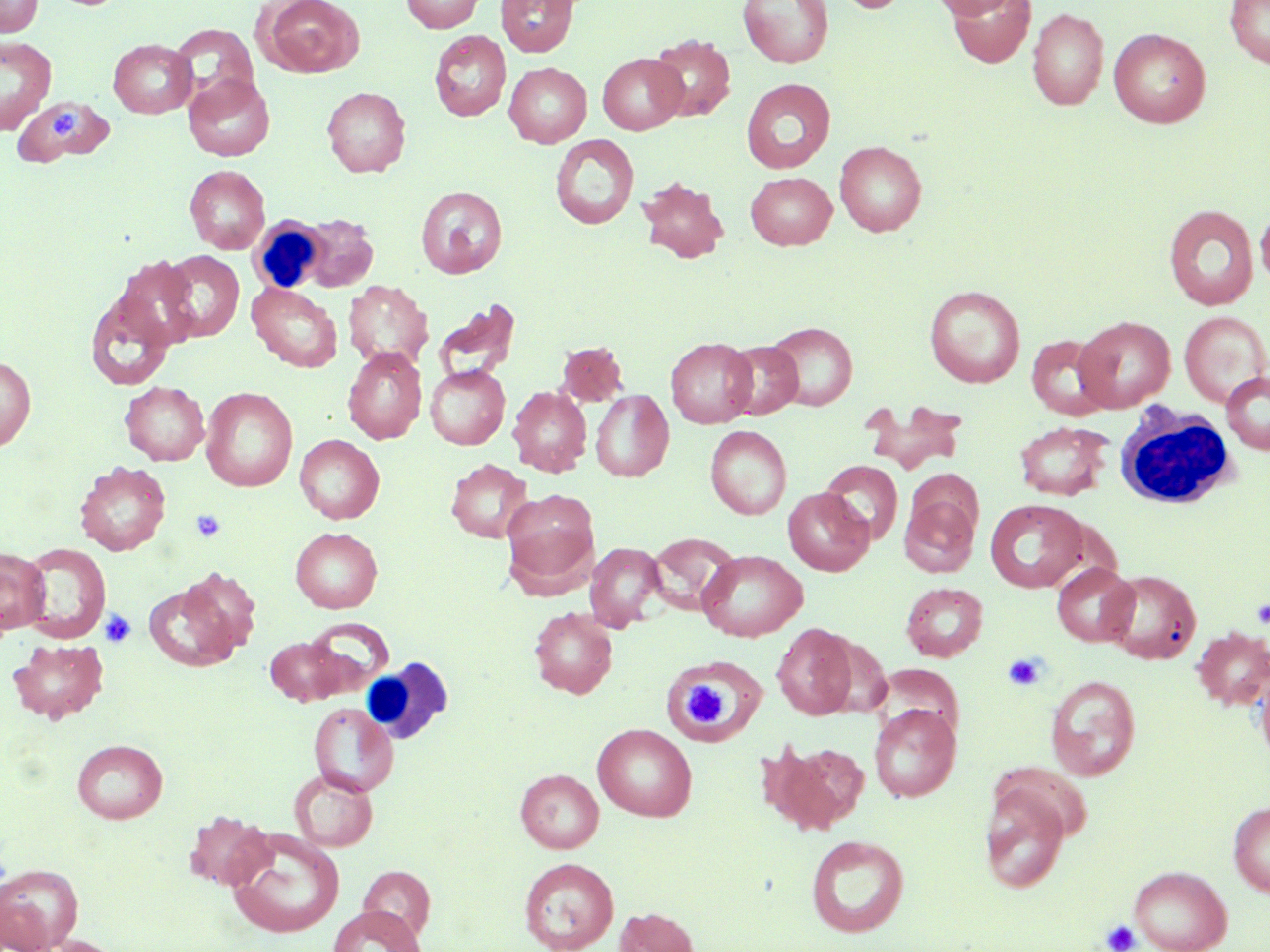
Summary:
  - Coordinate format: approximate bounding boxes as (x1,y1)-(x2,y2) corner pairs in pixels
  - White blood cell locations: (249,216)-(330,295), (1115,401)-(1241,510), (361,657)-(453,746)
  - Platelet locations: (191,509)-(226,542), (1251,599)-(1270,628), (99,610)-(136,647), (1002,652)-(1047,692), (685,681)-(726,726), (1101,919)-(1141,952)
  - Uninfected red blood cell locations: (0,0)-(42,36), (257,0)-(364,78), (401,0)-(485,32), (496,0)-(579,57), (739,0)-(833,68), (829,0)-(910,14), (930,0)-(1018,19), (1225,0)-(1270,68), (946,1)-(1035,68), (1027,6)-(1108,111), (169,22)-(259,105), (1108,28)-(1211,128), (429,29)-(511,121), (648,34)-(736,122), (0,36)-(55,134), (109,38)-(197,118), (598,53)-(687,135), (504,62)-(591,147), (183,74)-(275,161), (741,78)-(835,173), (322,86)-(410,177), (14,96)-(114,167), (550,133)-(639,230), (835,140)-(926,236), (184,165)-(269,254), (745,172)-(837,249), (638,177)-(728,263), (416,186)-(507,278), (1163,203)-(1258,310), (1256,207)-(1270,291), (298,212)-(378,292), (160,250)-(244,342), (115,257)-(198,348), (342,280)-(432,371), (247,282)-(343,372), (924,284)-(1025,387), (85,290)-(176,391), (432,297)-(522,385), (1179,310)-(1270,406), (1074,316)-(1175,412), (764,321)-(858,411), (1025,334)-(1113,420), (666,337)-(757,428), (721,340)-(803,419), (555,341)-(628,407), (343,347)-(426,444), (0,355)-(36,451), (425,365)-(510,449), (1221,371)-(1270,454), (120,381)-(209,465), (507,385)-(592,477), (201,387)-(298,492), (590,389)-(673,482), (866,402)-(967,475), (1014,421)-(1115,501), (705,425)-(791,519), (295,434)-(384,524), (446,458)-(532,542), (819,460)-(903,545), (75,461)-(170,555), (783,488)-(874,575), (501,489)-(599,590), (899,493)-(980,578), (985,499)-(1090,593), (290,526)-(382,612), (646,532)-(740,616), (21,542)-(110,642), (585,542)-(667,631), (0,547)-(50,635), (697,550)-(808,641), (1051,562)-(1139,646), (177,567)-(262,655), (1102,569)-(1201,664), (144,578)-(244,672), (901,582)-(988,661), (529,607)-(618,699), (306,618)-(393,694), (772,622)-(858,720), (1192,627)-(1270,711), (265,637)-(345,705), (8,638)-(108,724), (665,661)-(757,743), (1254,661)-(1270,771), (877,664)-(965,740), (1045,675)-(1141,781), (309,702)-(398,797), (868,703)-(961,802), (593,724)-(697,821), (72,738)-(168,823), (763,739)-(870,835), (290,769)-(378,851), (515,769)-(604,853), (980,781)-(1070,894), (1228,800)-(1270,897), (184,811)-(274,891), (227,829)-(345,938), (805,834)-(910,937), (518,857)-(619,952), (0,863)-(83,950), (1129,864)-(1232,952), (359,865)-(434,944), (329,905)-(425,952), (614,906)-(700,952), (36,935)-(129,952)
  - Slide-level diagnosis: negative for blood parasites
  - Field of view: single
  - Image size: 1270×952 pixels
  - Preparation: thin blood film
  - Stain: May-Grünwald-Giemsa
  - Magnification: 1000x
  - Modality: light microscopy